Give the position of every Plasmodium parasite visible.
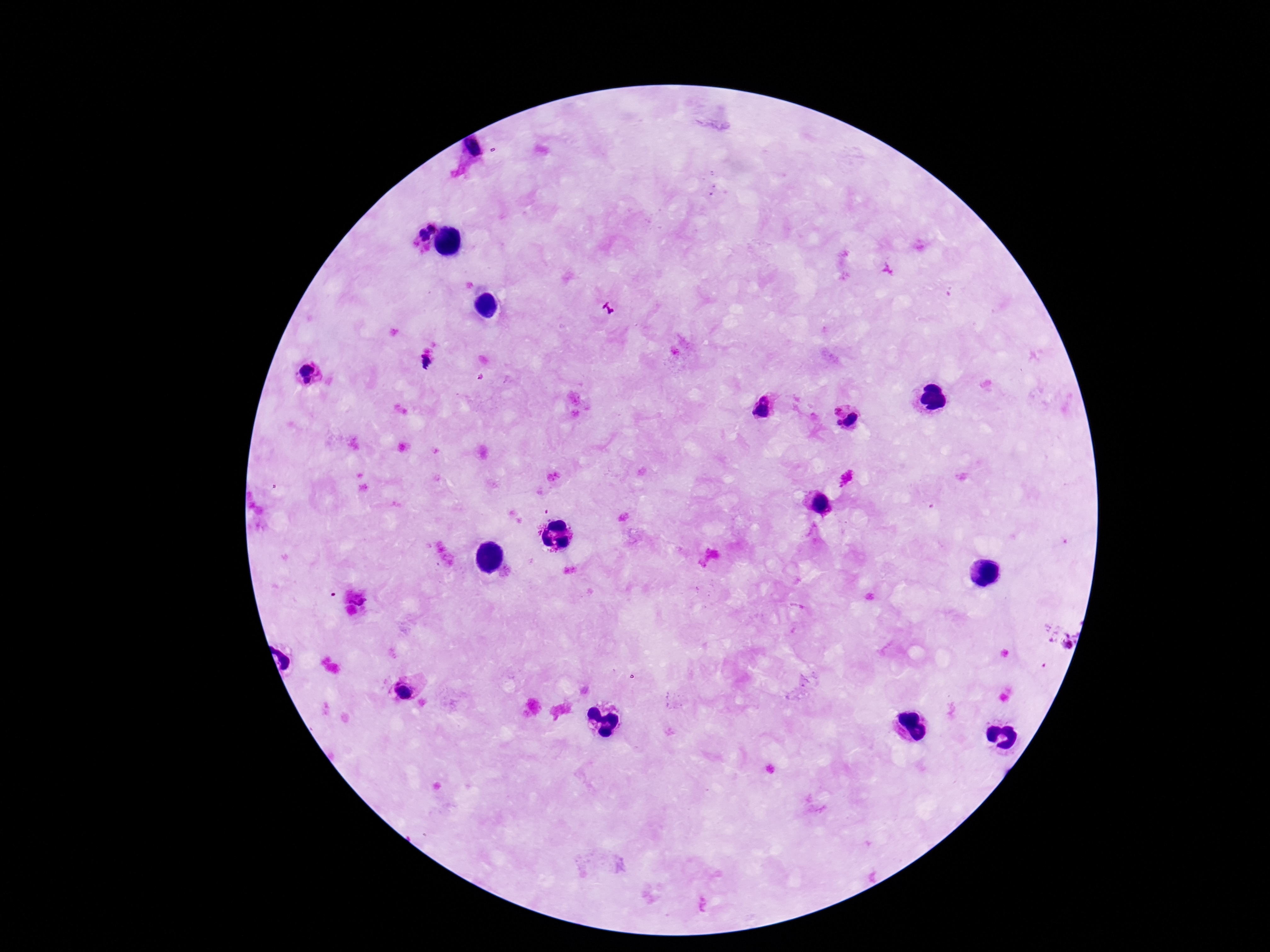
Approximate object centers, in pixels from the top-left corner.
Plasmodium parasites: (x=474, y=151), (x=423, y=230), (x=426, y=362), (x=304, y=367), (x=307, y=381), (x=763, y=397), (x=838, y=408), (x=760, y=411), (x=853, y=420), (x=839, y=422), (x=820, y=504), (x=358, y=597), (x=1069, y=641), (x=403, y=690).

Image is 1270×952 pixels. Thick peripheral-blood smear. 100x magnification. Patient malaria status: positive. Giemsa stain. Photographed through the microscope eyepiece with a smartphone camera. Single field of view.